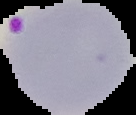
The area outside the segmented cell region is set to black. Result: Plasmodium parasites detected. From a thin blood smear. Image is 136×115 pixels.